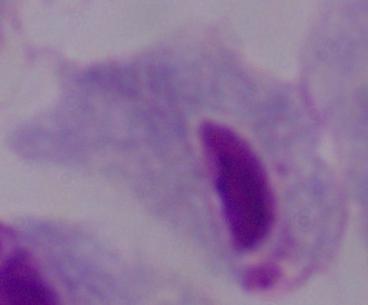 Photomicrograph. A trichomonad is shown. Captured at 1000x magnification.